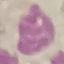
Summary:
  - Result: no malaria parasites seen
  - Capture: smartphone through the microscope eyepiece
  - Stain: Giemsa
  - Image type: cell patch, automatically extracted from a larger field of view and resized to 64 × 64 pixels
  - Preparation: thin blood film